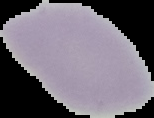
Summary:
  - Preparation: thin blood smear
  - Result: no Plasmodium parasites seen
  - Image type: cell region segmented out of the field of view; surrounding area masked to black
  - Image size: 154×118 pixels